Name the cell type shown.
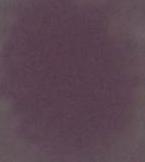
This is an erythrocyte.

Photomicrograph. 1000x magnification.